Classify this cell by malaria status.
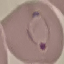

Parasitized.

capture = smartphone through the microscope eyepiece
stain = Giemsa
preparation = thin smear
image type = cell patch, automatically extracted from a larger field of view and resized to 64 × 64 pixels